Outline each blood parasite and name the species.
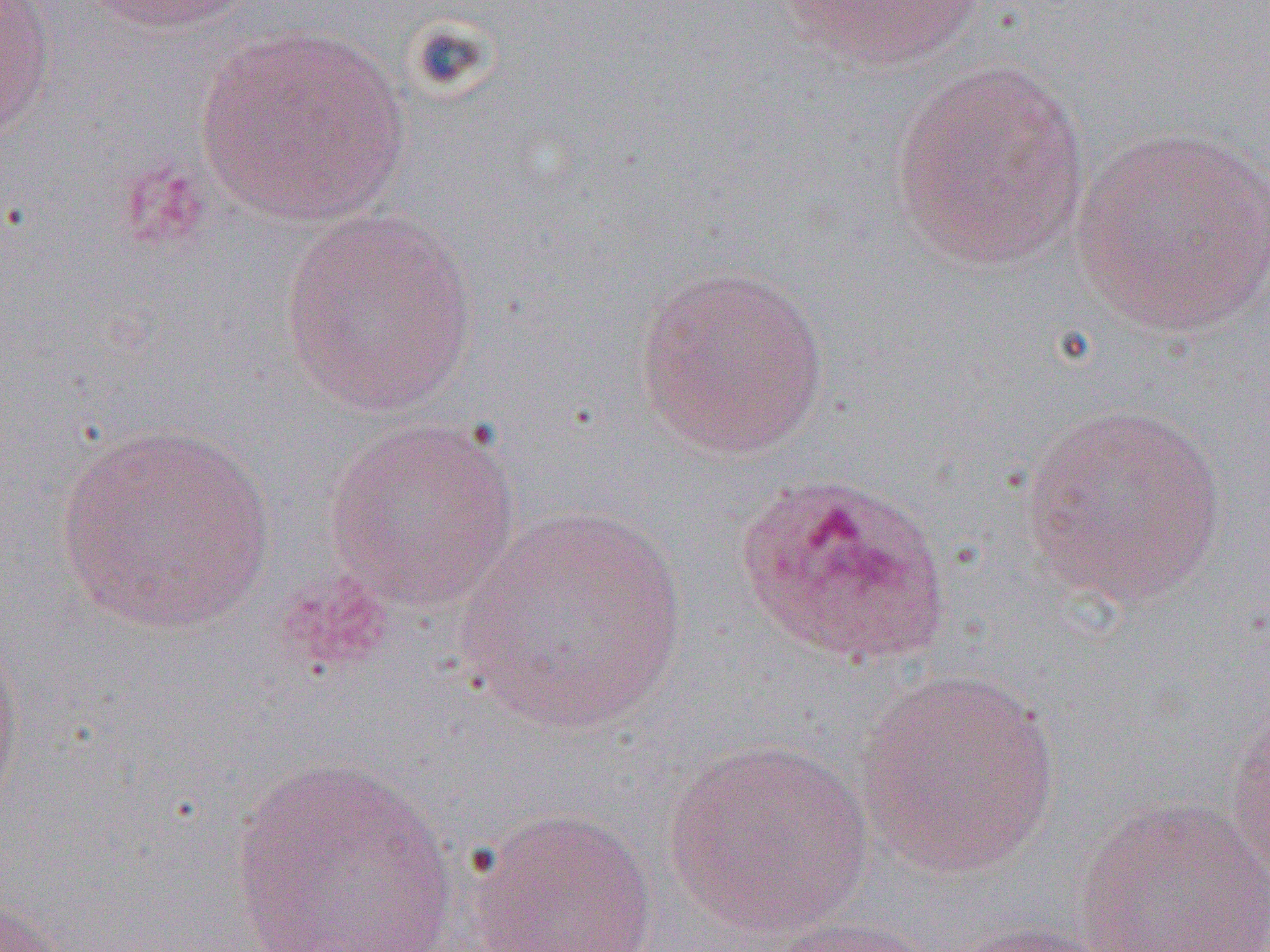

Approximate bounding boxes as (x1,y1)-(x2,y2) corner pairs in pixels.
Plasmodium ovale-infected red blood cells: (733,470)-(952,669).
No Plasmodium falciparum, Plasmodium malariae, Plasmodium vivax, Babesia divergens, or Trypanosoma brucei observed.

Uninfected red blood cell locations: (80,0)-(263,35), (778,0)-(990,73), (0,1)-(57,144), (194,24)-(409,227), (887,60)-(1092,272), (1070,126)-(1270,340), (276,208)-(480,417), (634,263)-(831,459), (1018,403)-(1230,607), (323,416)-(522,612), (55,421)-(276,636), (460,504)-(688,735), (0,628)-(25,815), (854,669)-(1064,879), (1225,694)-(1270,885), (664,737)-(873,938), (227,754)-(460,951), (1071,796)-(1270,952), (463,806)-(660,952), (0,897)-(67,952), (762,915)-(945,952), (940,920)-(1126,951). Slide-level diagnosis: Plasmodium ovale. Single field of view. Thin blood smear. 1000x magnification. Image is 1270×952 pixels. Optical microscopy.